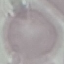
Malaria status: uninfected. Acquired by smartphone through the microscope eyepiece. Giemsa-stained preparation. Thin smear of blood. Automatically extracted cell patch, resized to 64 × 64 pixels.